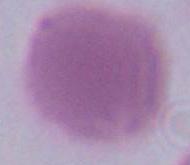

Summary:
  - Magnification: 1000x
  - Modality: photomicrograph
  - Identification: red blood cell